Describe the morphology of the red blood cells.
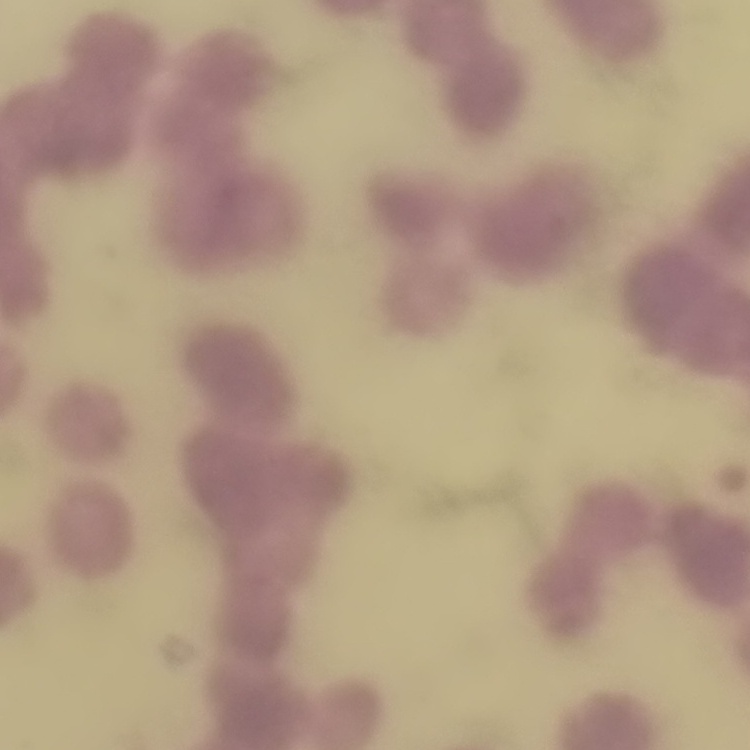

Rouleaux formation.

Summary:
  - Preparation: thin blood film
  - Stain: Field's or Giemsa
  - Image type: one tile cut from a larger photomicrograph